Give the position of every Plasmodium parasite.
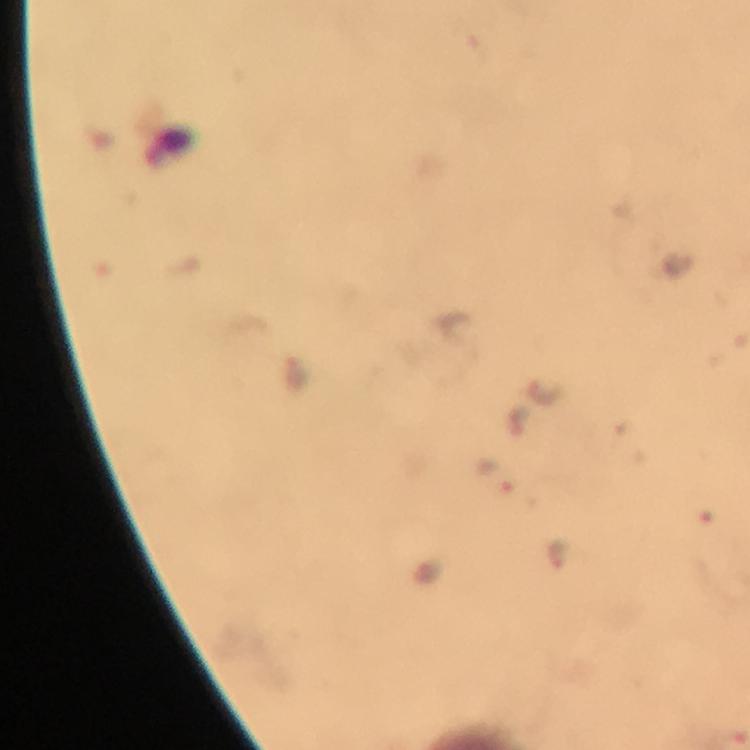

Approximate object centers, in pixels from the top-left corner.
Plasmodium parasites: (x=495, y=473), (x=560, y=551).

context = from a malaria diagnostic workup
immersion oil = used
stain = Giemsa
preparation = thick smear
capture = smartphone mounted on the microscope
image size = 750×750 pixels
cropped from = a single field of view
magnification = 100x